Describe the morphology of the red blood cells.
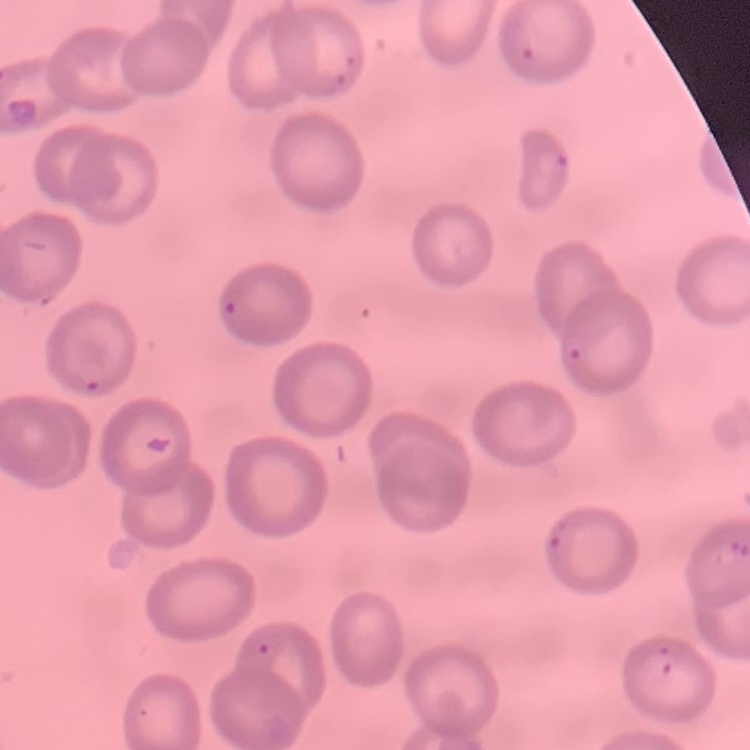

No rouleaux formation.

{
  "stain": "Field's or Giemsa",
  "preparation": "thin peripheral smear",
  "image_type": "square crop of a larger photomicrograph"
}